Locate every Plasmodium parasite.
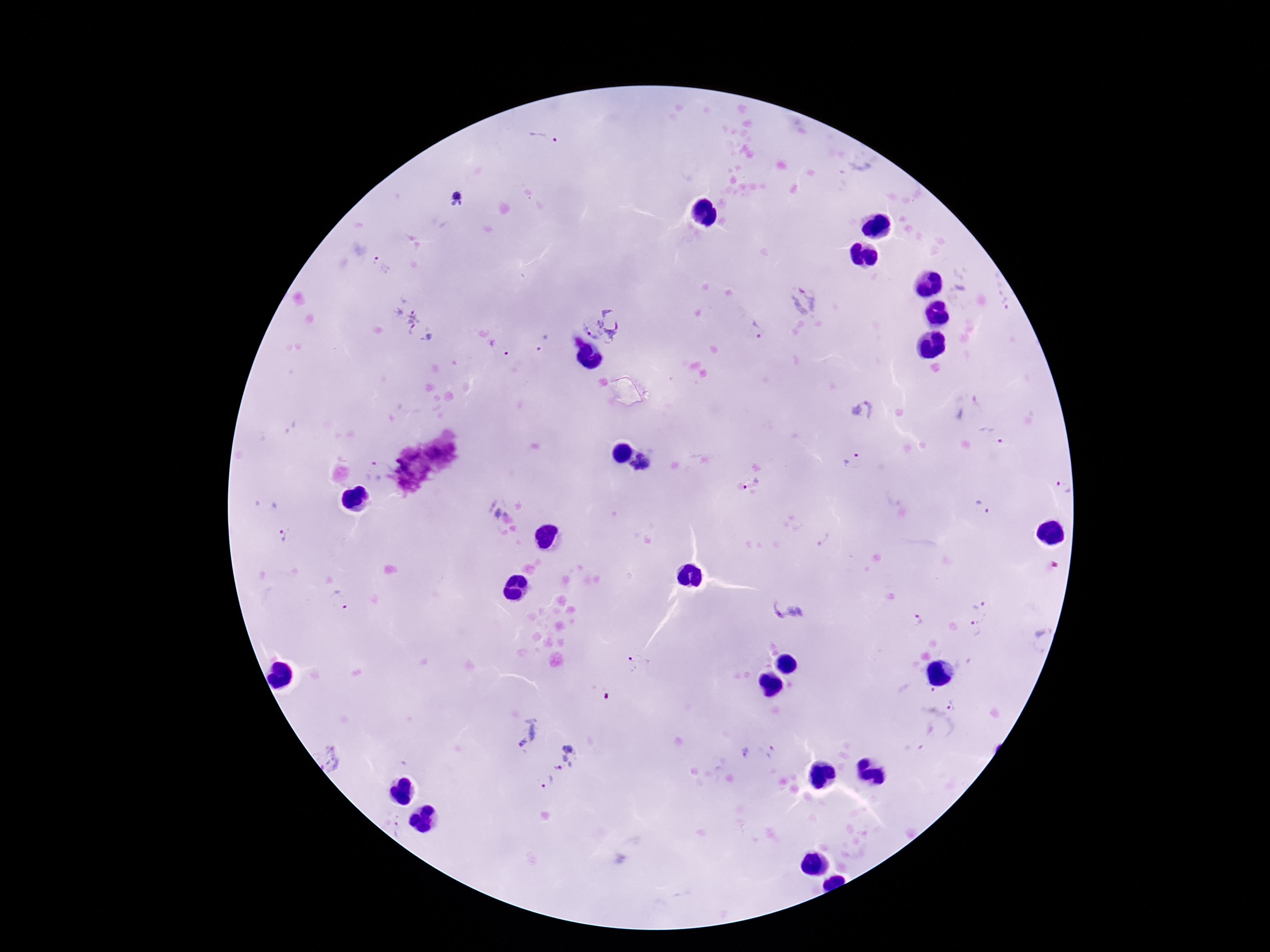
Approximate object centers, in pixels from the top-left corner.
Plasmodium parasites: (x=547, y=138), (x=456, y=199), (x=381, y=267), (x=804, y=300), (x=400, y=317), (x=602, y=326), (x=756, y=330), (x=428, y=337), (x=544, y=343), (x=497, y=347), (x=862, y=410), (x=992, y=435), (x=853, y=460), (x=640, y=463), (x=373, y=468), (x=752, y=483), (x=1063, y=488), (x=267, y=503), (x=498, y=504), (x=983, y=509), (x=286, y=533), (x=978, y=603), (x=338, y=604), (x=789, y=609), (x=917, y=620), (x=975, y=626), (x=641, y=667), (x=953, y=706), (x=523, y=731), (x=745, y=751), (x=767, y=752), (x=329, y=757), (x=563, y=757), (x=546, y=780), (x=399, y=830).

Thick blood smear. Giemsa-stained preparation. Image is 1270×952 pixels. Single field of view. Patient malaria status: positive. Photographed through the microscope eyepiece with a smartphone camera. 100x magnification.